Outline each Plasmodium malariae-infected red blood cell.
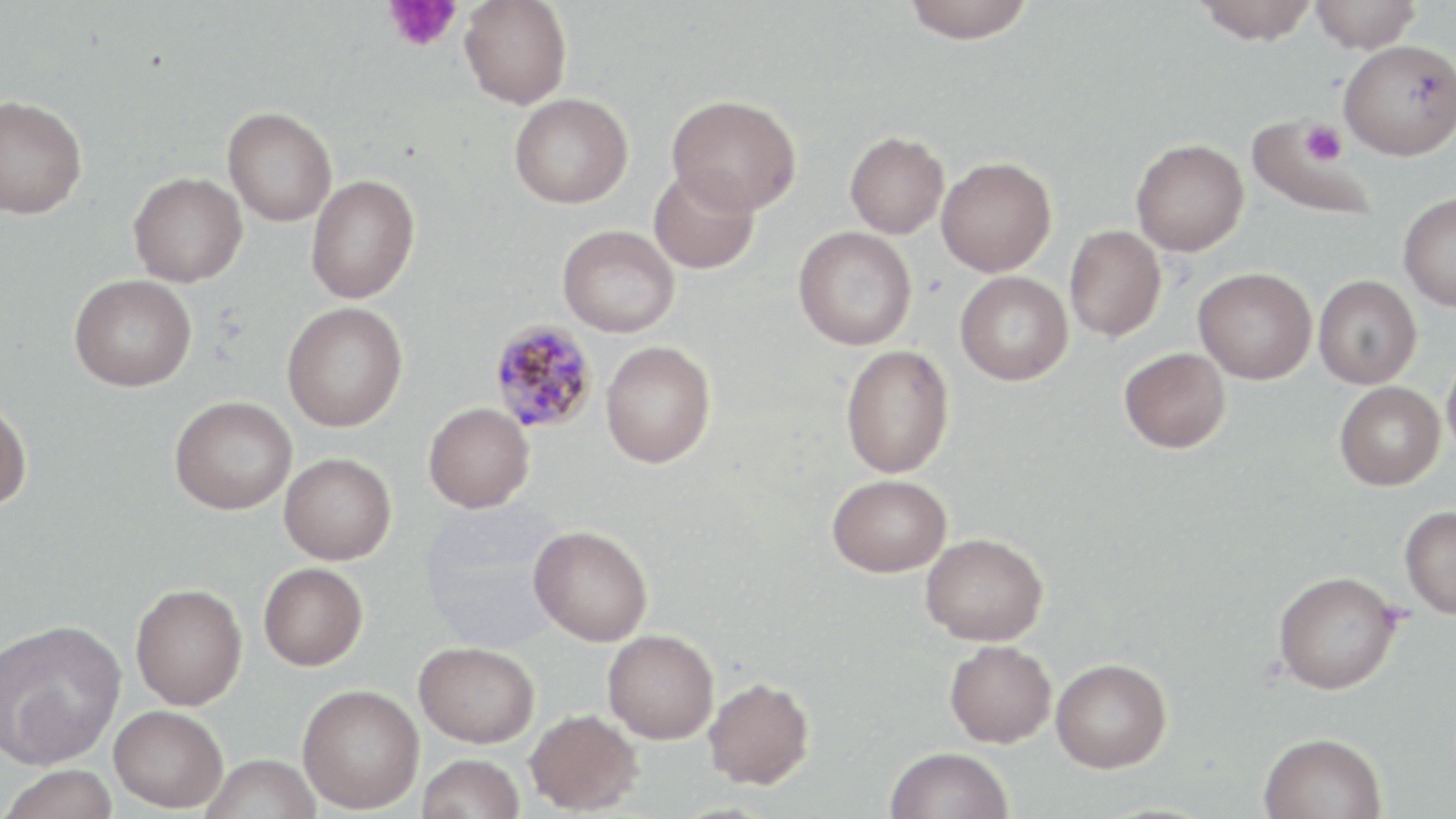
Approximate bounding boxes as [x1, y1, x2, y2] in pixels.
Plasmodium malariae-infected red blood cells: [488, 320, 598, 435].

Uninfected red blood cell locations: [902, 0, 1035, 44], [1194, 0, 1318, 45], [1310, 0, 1422, 53], [460, 1, 572, 109], [1339, 39, 1456, 159], [509, 93, 634, 208], [666, 94, 802, 215], [0, 95, 87, 218], [222, 106, 337, 226], [1246, 117, 1372, 220], [845, 131, 949, 238], [1131, 139, 1248, 256], [936, 156, 1056, 277], [648, 169, 760, 274], [128, 172, 247, 287], [306, 174, 420, 304], [1398, 194, 1456, 311], [557, 225, 680, 337], [1064, 225, 1166, 342], [793, 226, 917, 350], [1194, 267, 1316, 384], [955, 271, 1073, 385], [69, 275, 196, 392], [1313, 275, 1422, 389], [281, 302, 408, 432], [600, 341, 715, 467], [840, 345, 954, 478], [1119, 347, 1230, 453], [1442, 353, 1456, 466], [1334, 381, 1445, 490], [170, 396, 297, 514], [0, 397, 31, 511], [423, 402, 535, 513], [279, 452, 396, 565], [827, 473, 952, 577], [1399, 505, 1456, 618], [529, 525, 653, 645], [921, 532, 1048, 645], [258, 562, 368, 670], [1273, 571, 1400, 694], [130, 583, 247, 710], [1, 618, 125, 770], [603, 629, 719, 744], [944, 639, 1057, 747], [413, 641, 539, 747], [1051, 658, 1172, 772], [703, 677, 814, 789], [297, 684, 424, 813], [109, 705, 228, 812], [525, 708, 643, 815], [1258, 731, 1388, 819], [886, 747, 1013, 819], [418, 753, 525, 819], [202, 754, 321, 818], [1, 764, 120, 819]. Platelet locations: [383, 1, 460, 52], [1300, 120, 1347, 168]. Slide-level diagnosis: Plasmodium malariae. Light microscopy. May-Grünwald-Giemsa stain. Thin blood smear. 1000x magnification. Image is 1456×819 pixels. Single field of view.